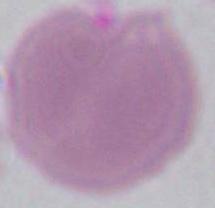

modality = micrograph
magnification = 1000x
identification = red blood cell